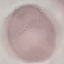

Malaria status: uninfected. Giemsa stain. Photographed with a smartphone camera at the microscope eyepiece. Automatically extracted cell patch, resized to 64 × 64 pixels. Thin blood smear.